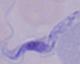

identification: trypanosome
modality: micrograph
magnification: 1000x